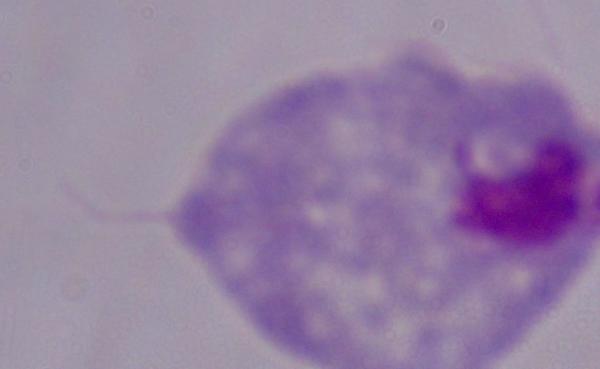

Summary:
  - Modality: micrograph
  - Identification: trichomonad
  - Magnification: 1000x